Point out leukocytes.
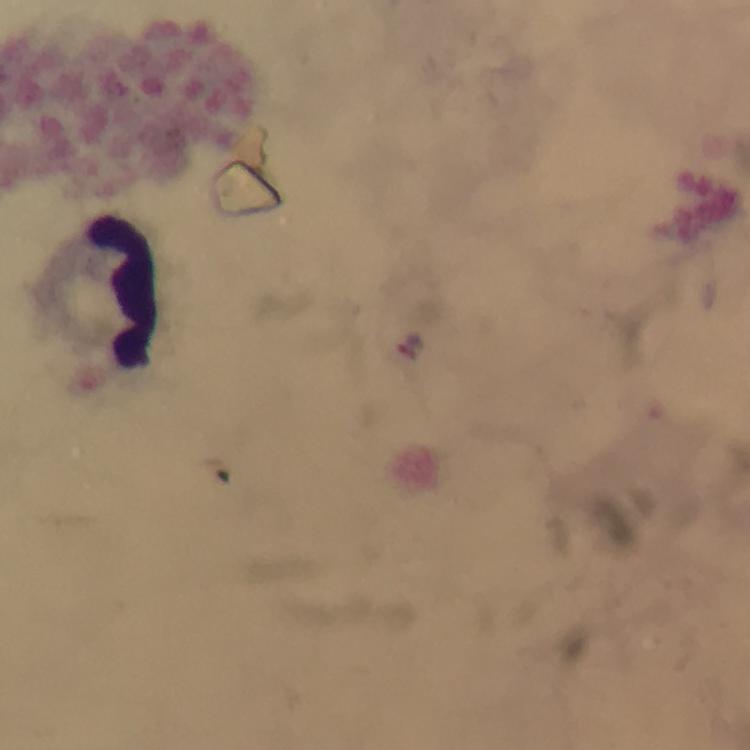
Approximate centers as {x, y} in pixels.
Leukocytes: {125, 290}.

capture = smartphone photograph through a microscope
image size = 750×750 pixels
magnification = 100x
Plasmodium parasites = none detected
immersion oil = used
preparation = thick blood smear
context = from a diagnostic examination for malaria
cropped from = one field of view
stain = Giemsa